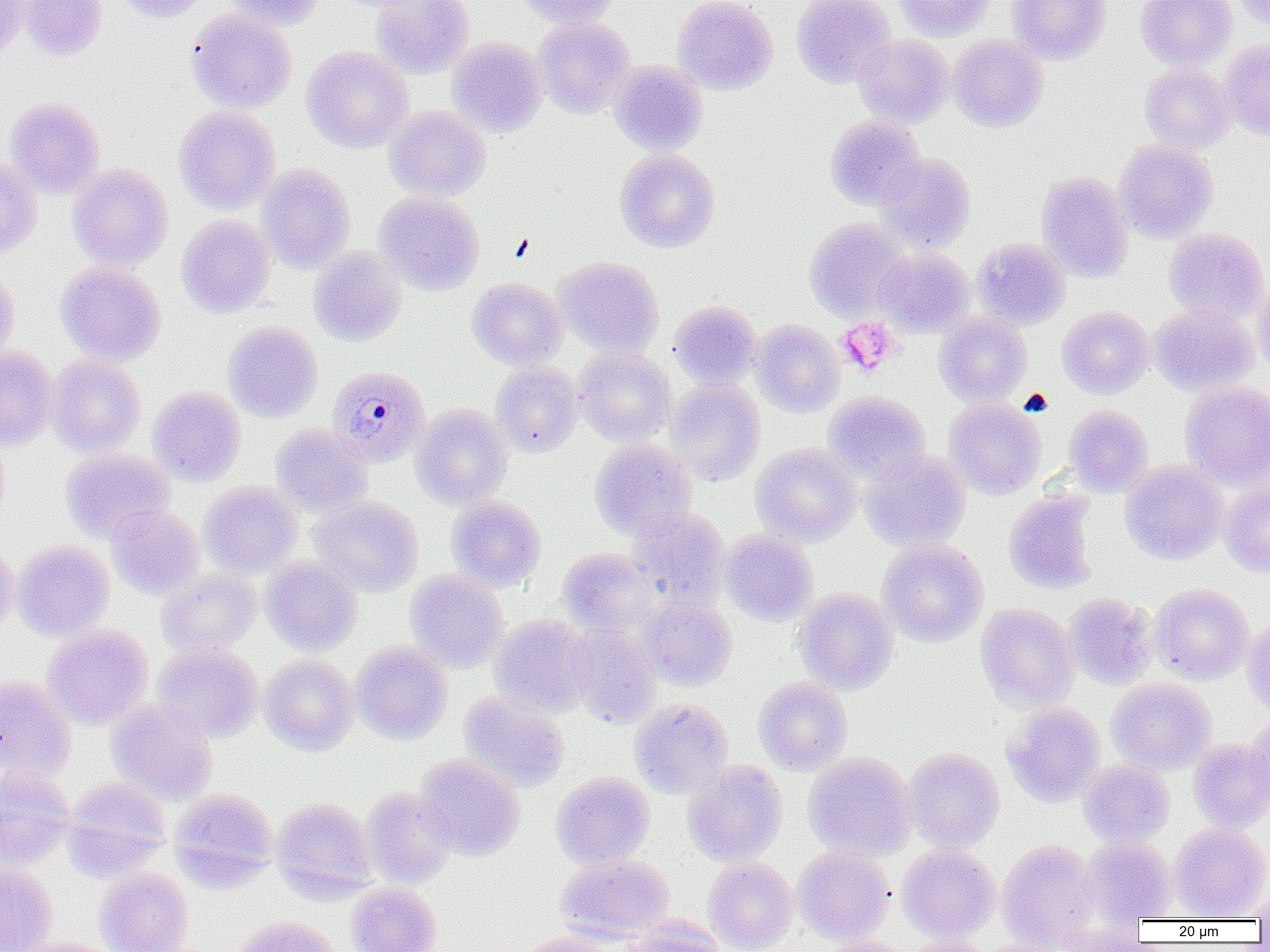

plasmodium_malariae_infected_red_blood_cell_locations: 'approximate bounding boxes as (x1,y1)-(x2,y2) corner pairs in pixels: (328,366)-(431,467)'
slide_level_diagnosis: Plasmodium malariae
magnification: 1000x
platelet_locations: 'approximate bounding boxes as (x1,y1)-(x2,y2) corner pairs in pixels: (837,317)-(900,376)'
image_size: 1270×952 pixels
modality: optical microscopy
preparation: thin blood smear
field_of_view: one of a larger specimen
uninfected_red_blood_cell_locations: 'approximate bounding boxes as (x1,y1)-(x2,y2) corner pairs in pixels: (0,0)-(30,57), (21,0)-(106,60), (108,0)-(206,23), (221,0)-(325,30), (372,0)-(474,78), (515,0)-(618,28), (673,0)-(777,94), (792,0)-(896,88), (893,0)-(994,42), (1007,0)-(1111,64), (1136,0)-(1236,70), (1235,0)-(1269,28), (186,8)-(296,113), (534,16)-(635,118), (854,34)-(954,128), (948,34)-(1048,132), (447,37)-(547,137), (1220,40)-(1270,141), (301,45)-(414,153), (609,61)-(707,155), (1139,62)-(1235,152), (4,98)-(105,198), (173,106)-(281,214), (384,106)-(491,201), (825,115)-(925,210), (1114,139)-(1218,242), (614,149)-(720,252), (877,153)-(976,252), (0,156)-(42,259), (257,163)-(355,273), (68,164)-(173,270), (1035,170)-(1133,282), (374,192)-(484,294), (177,215)-(276,318), (804,217)-(911,321), (1163,227)-(1268,322), (973,237)-(1071,330), (308,245)-(407,346), (874,248)-(975,337), (554,256)-(664,356), (55,262)-(166,365), (0,268)-(19,366), (467,277)-(566,369), (1252,278)-(1270,379), (669,300)-(762,389), (1150,304)-(1257,395), (1057,305)-(1155,399), (934,311)-(1031,406), (751,319)-(844,417), (223,321)-(323,422), (0,346)-(60,451), (574,346)-(676,445), (47,355)-(146,457), (491,360)-(583,457), (667,378)-(765,486), (1180,380)-(1270,488), (148,386)-(246,486), (824,391)-(930,482), (944,398)-(1047,500), (411,403)-(512,508), (1063,404)-(1153,496), (270,423)-(372,516), (589,439)-(696,539), (751,442)-(861,546), (60,448)-(175,543), (861,449)-(970,551), (1120,460)-(1228,564), (1218,480)-(1270,578), (199,481)-(303,577), (1003,490)-(1099,594), (446,495)-(546,591), (310,496)-(423,596), (106,504)-(204,599), (628,505)-(730,603), (720,528)-(819,626), (0,539)-(18,638), (878,539)-(989,647), (12,540)-(114,641), (557,547)-(659,637), (260,556)-(362,655), (156,568)-(261,656), (406,569)-(508,672), (1150,583)-(1254,684), (793,588)-(899,695), (1064,593)-(1158,689), (639,594)-(738,691), (975,603)-(1079,710), (489,615)-(596,716), (1241,618)-(1270,719), (43,623)-(153,729), (567,623)-(662,727), (351,640)-(453,744), (152,642)-(264,742), (259,653)-(358,755), (0,674)-(77,782), (753,676)-(852,775), (1107,677)-(1216,775), (458,690)-(571,792), (106,697)-(218,804), (629,698)-(733,798), (1002,701)-(1106,806), (1246,713)-(1270,811), (1187,738)-(1270,831), (904,746)-(1005,851), (803,752)-(916,860), (415,754)-(525,861), (682,759)-(788,866), (1079,760)-(1175,847), (0,765)-(75,869), (551,772)-(655,869), (64,776)-(171,873), (361,787)-(457,889), (169,788)-(278,887), (271,797)-(377,900), (1169,822)-(1270,919), (1081,835)-(1176,923), (997,839)-(1100,950), (898,843)-(1000,943), (792,845)-(894,945), (555,853)-(675,943), (703,857)-(798,952), (0,861)-(58,952), (95,867)-(193,952), (345,881)-(442,952), (1247,893)-(1269,923), (230,915)-(342,952), (621,917)-(728,951), (510,933)-(620,952), (813,936)-(914,952), (902,937)-(997,952), (10,938)-(126,952), (979,939)-(1077,952)'